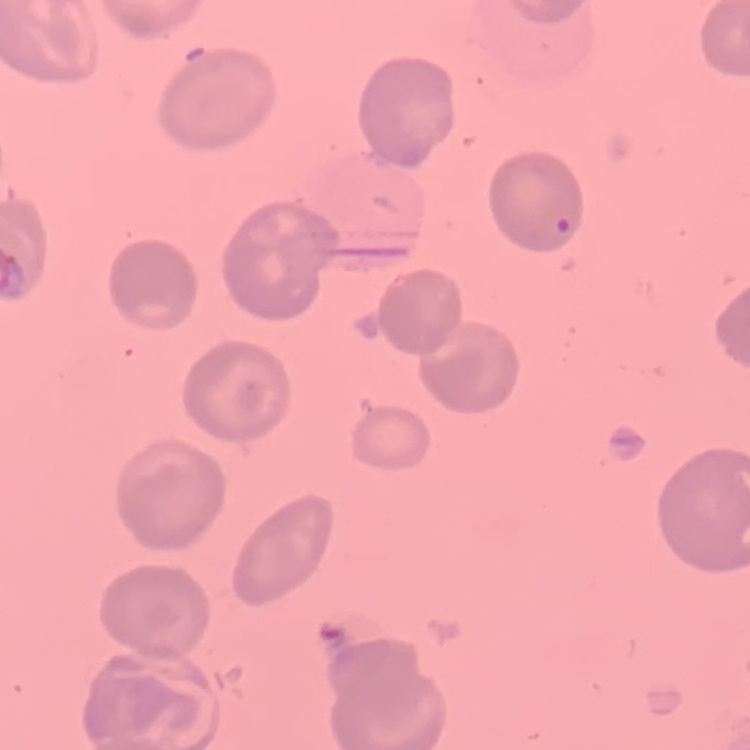

Summary:
  - Red blood cell morphology: no rouleaux formation
  - Image type: square crop of a larger photomicrograph
  - Preparation: thin blood smear
  - Stain: Field's or Giemsa